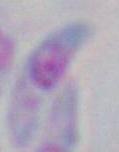

identification: Toxoplasma gondii
magnification: 1000x
modality: photomicrograph